Name the parasite shown.
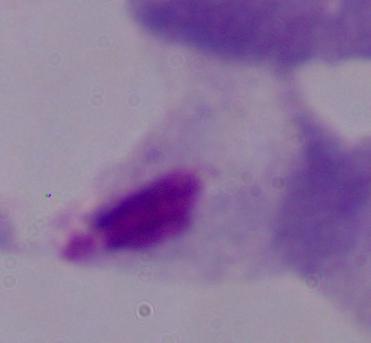
A trichomonad.

Captured at 1000x magnification. Photomicrograph.